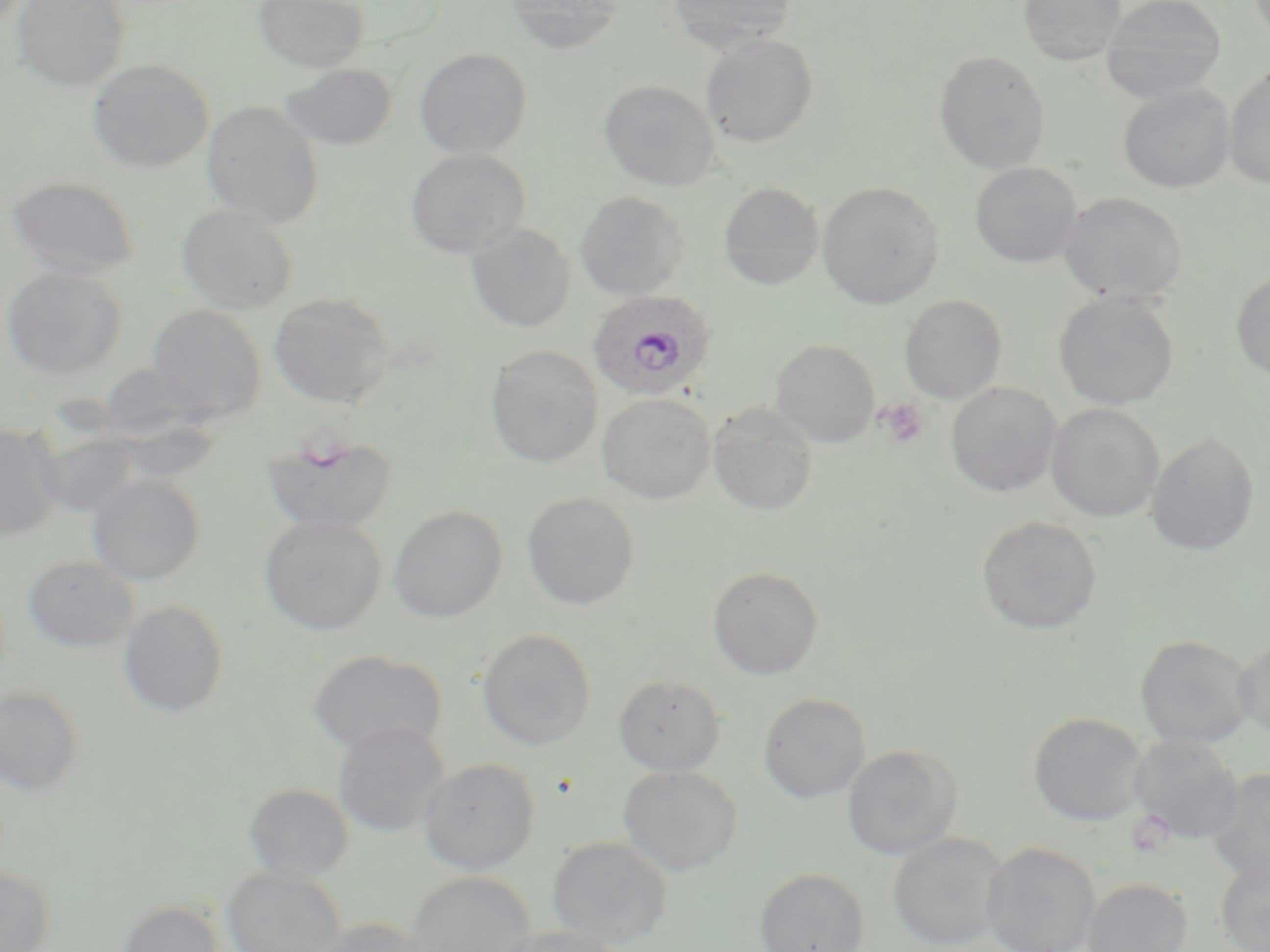
Approximate bounding boxes as named x1/y1/x2/y2 corners in pixels. Platelet locations: (x1=877, y1=399, x2=929, y2=449). Uninfected red blood cell locations: (x1=12, y1=0, x2=130, y2=91), (x1=253, y1=0, x2=369, y2=72), (x1=504, y1=0, x2=625, y2=55), (x1=668, y1=0, x2=797, y2=53), (x1=1019, y1=0, x2=1126, y2=65), (x1=1102, y1=0, x2=1226, y2=103), (x1=701, y1=34, x2=818, y2=147), (x1=414, y1=48, x2=533, y2=159), (x1=935, y1=51, x2=1050, y2=174), (x1=88, y1=59, x2=214, y2=173), (x1=281, y1=62, x2=397, y2=151), (x1=1223, y1=65, x2=1270, y2=190), (x1=600, y1=80, x2=720, y2=190), (x1=1118, y1=83, x2=1235, y2=193), (x1=202, y1=100, x2=325, y2=227), (x1=406, y1=147, x2=531, y2=258), (x1=970, y1=163, x2=1082, y2=268), (x1=7, y1=176, x2=141, y2=280), (x1=817, y1=182, x2=943, y2=309), (x1=719, y1=183, x2=824, y2=290), (x1=575, y1=191, x2=689, y2=300), (x1=1058, y1=192, x2=1187, y2=304), (x1=176, y1=203, x2=299, y2=313), (x1=465, y1=222, x2=575, y2=332), (x1=1, y1=265, x2=128, y2=380), (x1=1231, y1=271, x2=1270, y2=383), (x1=1053, y1=291, x2=1179, y2=411), (x1=268, y1=293, x2=394, y2=407), (x1=900, y1=295, x2=1006, y2=403), (x1=147, y1=304, x2=266, y2=424), (x1=770, y1=339, x2=880, y2=446), (x1=485, y1=345, x2=603, y2=467), (x1=946, y1=382, x2=1062, y2=496), (x1=597, y1=392, x2=715, y2=503), (x1=709, y1=403, x2=817, y2=516), (x1=1047, y1=404, x2=1165, y2=522), (x1=0, y1=423, x2=63, y2=543), (x1=262, y1=430, x2=398, y2=536), (x1=1145, y1=432, x2=1260, y2=556), (x1=87, y1=474, x2=206, y2=585), (x1=523, y1=492, x2=640, y2=609), (x1=389, y1=505, x2=508, y2=622), (x1=259, y1=515, x2=387, y2=635), (x1=976, y1=515, x2=1102, y2=634), (x1=23, y1=554, x2=139, y2=653), (x1=707, y1=566, x2=824, y2=679), (x1=119, y1=600, x2=230, y2=718), (x1=477, y1=628, x2=596, y2=749), (x1=1135, y1=634, x2=1256, y2=750), (x1=1234, y1=635, x2=1270, y2=738), (x1=307, y1=649, x2=447, y2=757), (x1=613, y1=673, x2=726, y2=776), (x1=0, y1=685, x2=85, y2=796), (x1=758, y1=692, x2=871, y2=803), (x1=1029, y1=712, x2=1147, y2=826), (x1=332, y1=720, x2=450, y2=838), (x1=1129, y1=735, x2=1243, y2=843), (x1=842, y1=745, x2=960, y2=860), (x1=418, y1=757, x2=540, y2=874), (x1=618, y1=765, x2=741, y2=876), (x1=1206, y1=768, x2=1270, y2=887), (x1=244, y1=783, x2=354, y2=881), (x1=888, y1=831, x2=1009, y2=950), (x1=547, y1=836, x2=673, y2=948), (x1=983, y1=842, x2=1101, y2=952), (x1=1215, y1=856, x2=1270, y2=952), (x1=0, y1=865, x2=56, y2=952), (x1=222, y1=867, x2=348, y2=952), (x1=754, y1=867, x2=870, y2=952), (x1=407, y1=872, x2=536, y2=952), (x1=1081, y1=877, x2=1193, y2=952), (x1=117, y1=900, x2=226, y2=952), (x1=312, y1=917, x2=431, y2=952), (x1=494, y1=925, x2=629, y2=952). Plasmodium ovale-infected red blood cell locations: (x1=587, y1=290, x2=716, y2=402). Slide-level diagnosis: Plasmodium ovale. May-Grünwald-Giemsa stain. Optical microscopy. One field of a larger specimen. Image is 1270×952 pixels. Thin blood film. Captured at 1000x magnification.